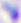
{
  "identification": "Toxoplasma gondii",
  "modality": "photomicrograph",
  "magnification": "400x"
}